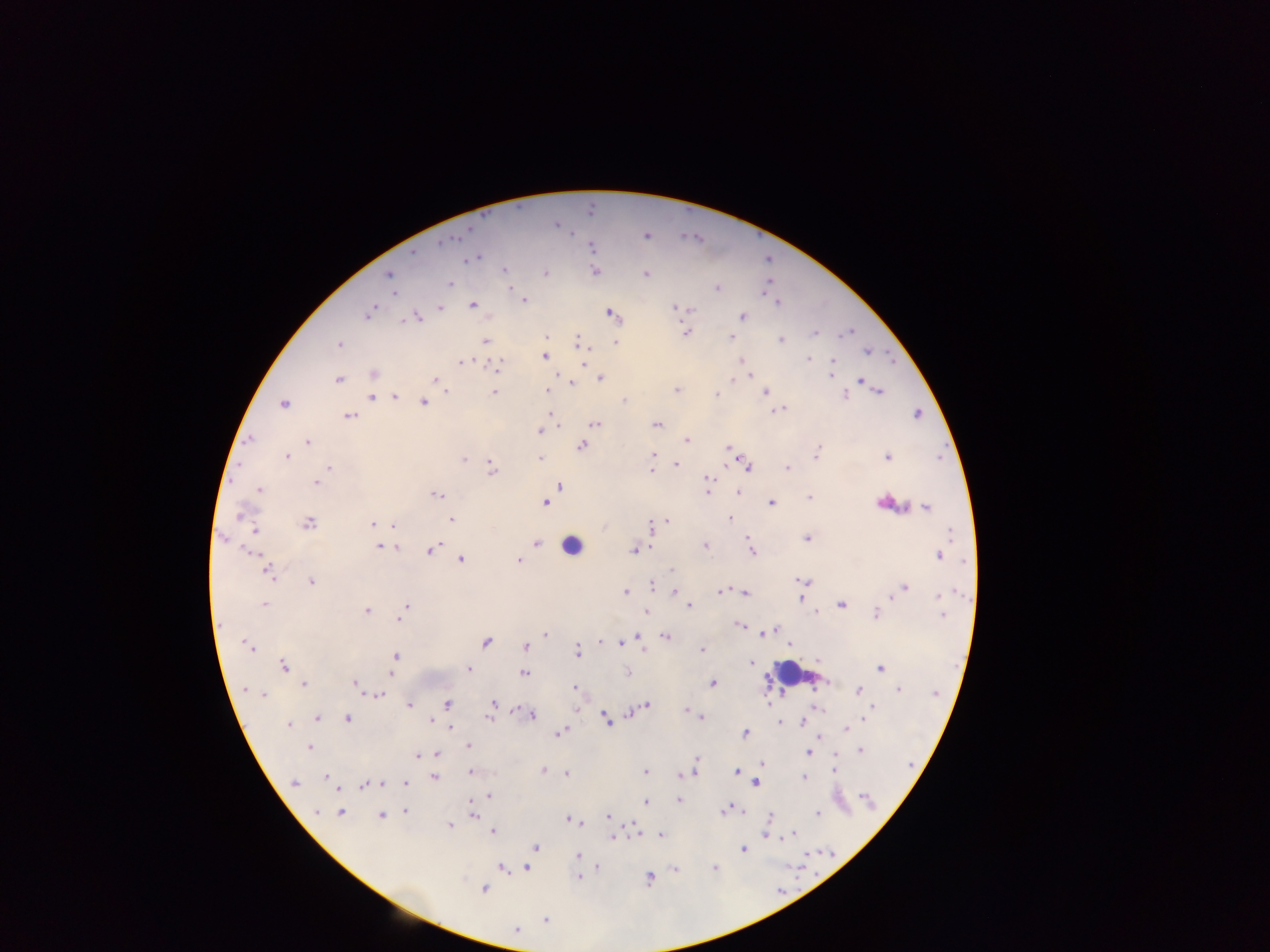
Approximate centers as x y in pixels.
Summary:
  - Malaria parasite locations: 556 225; 470 229; 646 235; 441 241; 592 247; 412 252; 475 258; 503 270; 596 271; 545 273; 647 274; 389 275; 449 283; 716 288; 393 293; 524 299; 776 303; 472 305; 440 306; 676 307; 370 312; 611 314; 742 316; 416 317; 815 333; 685 334; 730 338; 780 339; 485 342; 338 343; 579 343; 615 343; 868 351; 544 356; 583 360; 740 360; 807 360; 831 361; 461 362; 497 366; 830 370; 373 374; 559 377; 750 377; 830 377; 600 378; 337 379; 734 379; 434 380; 860 380; 440 384; 571 385; 493 391; 676 391; 878 391; 447 392; 547 392; 716 393; 764 393; 844 394; 370 397; 394 397; 623 400; 424 401; 283 404; 779 409; 917 414; 348 416; 553 418; 595 423; 656 424; 539 431; 249 439; 686 439; 308 442; 581 445; 726 448; 731 449; 817 452; 653 455; 287 456; 886 457; 540 458; 464 459; 726 463; 651 464; 676 464; 746 465; 329 467; 492 468; 787 469; 651 472; 706 479; 316 482; 559 486; 258 489; 737 491; 707 492; 437 494; 809 497; 543 502; 771 502; 888 503; 926 507; 241 515; 450 518; 730 518; 667 520; 307 523; 372 523; 393 526; 651 527; 255 529; 806 538; 223 539; 747 539; 376 541; 536 542; 704 545; 379 546; 395 547; 430 549; 634 550; 750 551; 253 553; 939 555; 461 559; 519 559; 671 570; 268 571; 803 581; 311 582; 651 585; 903 589; 674 591; 721 591; 625 592; 745 592; 800 597; 941 597; 265 605; 841 605; 406 606; 689 606; 366 611; 647 612; 815 613; 875 613; 941 614; 400 621; 740 625; 773 629; 764 632; 759 633; 546 634; 639 636; 667 636; 600 641; 485 642; 247 645; 789 646; 525 647; 643 647; 701 649; 577 651; 395 655; 750 662; 283 666; 469 668; 880 668; 393 672; 629 672; 523 673; 713 683; 304 684; 355 684; 574 688; 898 688; 247 690; 858 691; 264 694; 380 694; 493 702; 768 702; 446 703; 646 704; 410 705; 816 707; 871 707; 575 710; 686 710; 516 711; 628 713; 532 715; 699 715; 865 715; 489 717; 317 718; 347 718; 702 718; 431 719; 606 719; 802 721; 287 724; 779 724; 450 728; 845 729; 561 732; 745 733; 820 736; 467 745; 309 747; 860 750; 807 752; 436 754; 417 756; 696 761; 762 764; 834 770; 470 771; 542 771; 644 771; 693 771; 736 772; 566 773; 685 773; 679 774; 325 776; 433 776; 804 777; 756 782; 294 783; 381 783; 405 783; 364 786; 336 788; 488 795; 864 796; 678 799; 645 803; 725 810; 317 812; 404 812; 340 813; 742 813; 817 813; 472 814; 381 815; 608 816; 569 819; 580 822; 449 825; 492 831; 791 834; 636 835; 661 835; 766 835; 786 835; 613 836; 536 847; 743 850; 577 856; 526 867; 715 867; 502 868; 598 868; 675 868; 578 877; 648 877; 483 888; 545 920; 515 929
  - Leukocyte locations: 572 545; 796 674
  - Capture: mobile-phone photograph through a microscope
  - Image size: 1270×952 pixels
  - Country: Ghana
  - Field of view: single
  - Preparation: thick blood film